Name the cell type shown.
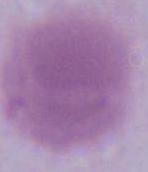
This is an erythrocyte.

magnification = 1000x
modality = photomicrograph